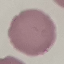

malaria status = uninfected
preparation = thin blood smear
image type = cell patch, automatically extracted from a larger field of view and resized to 64 × 64 pixels
stain = Giemsa
capture = smartphone through the microscope eyepiece